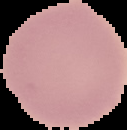
The area outside the segmented cell region is set to black. Malaria status: uninfected. From a thin blood smear. Image is 127×130 pixels.